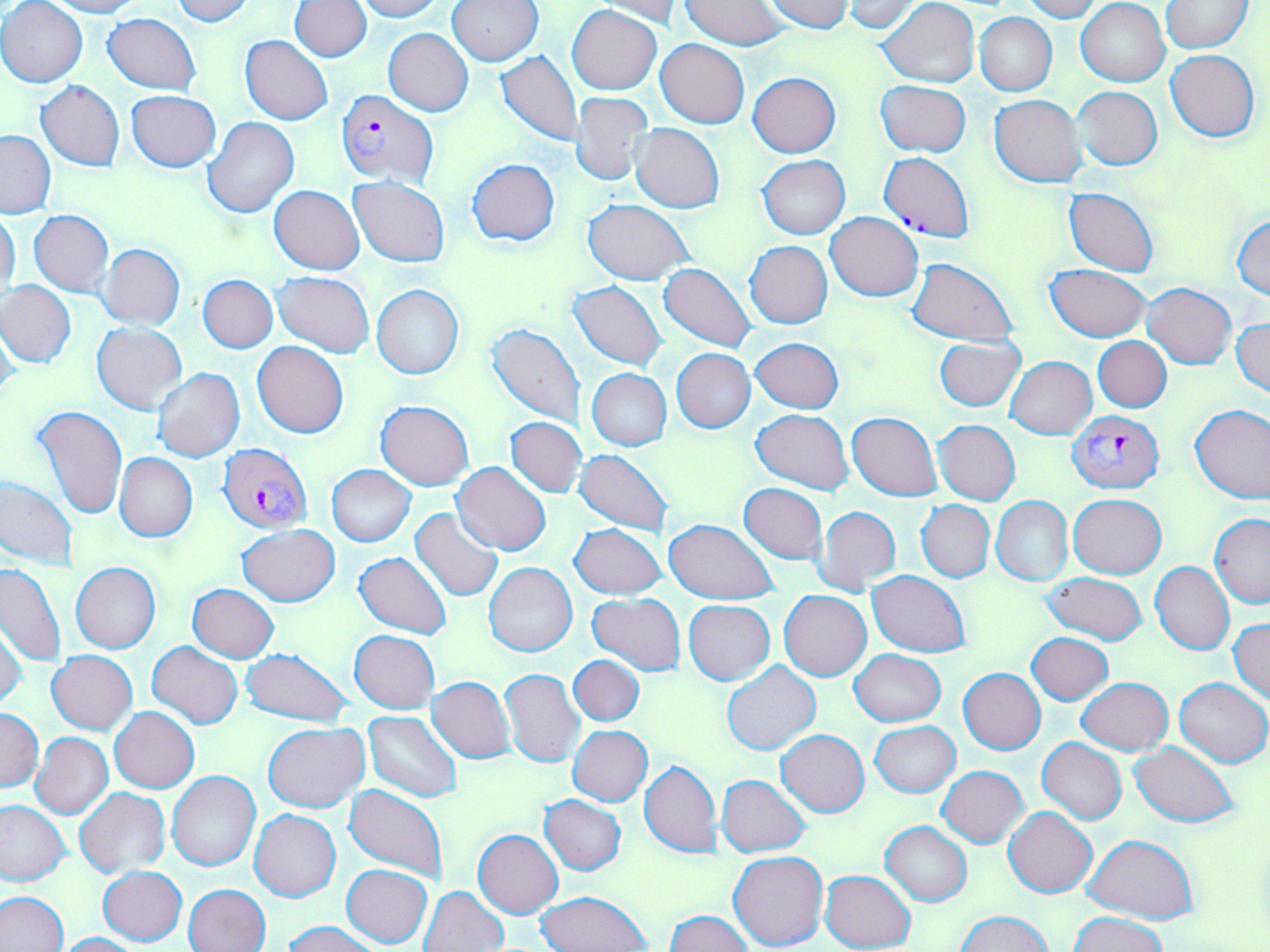 Approximate bounding boxes as [x1, y1, x2, y2] in pixels. Plasmodium falciparum-infected red blood cell locations: [336, 89, 438, 189], [1067, 413, 1164, 494], [225, 449, 319, 540]. Uninfected red blood cell locations: [40, 0, 143, 18], [170, 0, 252, 26], [356, 0, 444, 21], [448, 0, 543, 65], [763, 0, 856, 34], [1018, 0, 1101, 22], [1, 1, 88, 87], [290, 1, 371, 62], [583, 1, 684, 29], [846, 1, 925, 33], [1076, 1, 1170, 86], [1160, 1, 1252, 52], [680, 2, 790, 50], [878, 2, 980, 87], [567, 4, 661, 95], [103, 12, 202, 95], [974, 13, 1057, 96], [383, 28, 473, 116], [240, 35, 334, 125], [656, 39, 749, 128], [1166, 49, 1259, 141], [496, 50, 582, 146], [748, 73, 841, 157], [876, 80, 970, 156], [36, 81, 124, 171], [1072, 87, 1162, 169], [126, 90, 222, 171], [571, 92, 654, 185], [989, 95, 1087, 187], [203, 117, 298, 218], [632, 123, 723, 213], [1, 130, 55, 219], [879, 151, 974, 243], [758, 155, 850, 239], [467, 158, 560, 247], [348, 176, 449, 266], [269, 185, 364, 274], [1064, 188, 1159, 276], [582, 199, 693, 285], [1, 209, 20, 298], [28, 211, 114, 295], [825, 212, 923, 301], [1231, 214, 1270, 300], [745, 241, 833, 329], [98, 243, 185, 329], [907, 258, 1018, 344], [659, 263, 756, 351], [1046, 265, 1150, 341], [273, 271, 374, 356], [198, 274, 278, 352], [1, 279, 75, 368], [570, 281, 667, 369], [1141, 282, 1236, 368], [371, 284, 463, 379], [1233, 317, 1270, 397], [0, 318, 21, 409], [486, 322, 585, 427], [92, 323, 187, 414], [1092, 336, 1171, 412], [934, 337, 1026, 411], [751, 338, 843, 413], [252, 341, 349, 438], [671, 348, 755, 433], [1007, 356, 1096, 439], [152, 368, 245, 463], [587, 368, 672, 450], [375, 400, 474, 490], [1190, 403, 1270, 504], [33, 404, 127, 520], [751, 410, 854, 493], [848, 412, 942, 500], [506, 417, 586, 498], [933, 420, 1020, 505], [576, 448, 674, 536], [114, 453, 197, 541], [453, 462, 551, 557], [326, 465, 416, 546], [0, 477, 77, 568], [739, 483, 827, 563], [1068, 494, 1166, 578], [991, 496, 1073, 585], [917, 499, 995, 582], [814, 505, 901, 596], [410, 508, 503, 602], [1209, 515, 1270, 608], [664, 518, 778, 606], [569, 524, 669, 599], [238, 525, 339, 606], [353, 551, 453, 639], [70, 561, 161, 653], [1150, 561, 1234, 655], [484, 562, 577, 657], [0, 564, 65, 665], [867, 571, 970, 656], [1042, 572, 1146, 644], [189, 584, 279, 662], [779, 590, 872, 682], [589, 593, 685, 675], [683, 600, 775, 684], [1229, 618, 1270, 702], [0, 623, 28, 712], [349, 629, 440, 713], [1026, 632, 1113, 704], [148, 642, 242, 729], [241, 647, 352, 727], [849, 649, 945, 727], [46, 651, 137, 735], [862, 651, 950, 797], [568, 655, 644, 726], [722, 661, 819, 755], [499, 668, 585, 768], [958, 668, 1045, 754], [427, 677, 515, 764], [1077, 677, 1173, 755], [1175, 678, 1269, 767], [109, 707, 198, 793], [0, 709, 44, 791], [363, 711, 461, 802], [870, 721, 960, 796], [262, 722, 369, 812], [569, 724, 651, 806], [776, 730, 869, 817], [29, 732, 114, 819], [1037, 738, 1127, 824], [1130, 742, 1240, 827], [639, 760, 720, 858], [937, 766, 1027, 847], [167, 771, 261, 872], [717, 774, 810, 857], [343, 785, 450, 885], [75, 788, 170, 878], [539, 795, 627, 874], [0, 799, 71, 887], [1004, 806, 1097, 898], [250, 809, 341, 901], [880, 820, 971, 906], [473, 829, 562, 918], [1082, 834, 1197, 923], [729, 851, 829, 951], [342, 863, 432, 948], [97, 865, 187, 945], [820, 869, 915, 952], [183, 884, 271, 952], [420, 885, 508, 951], [1, 891, 68, 952], [537, 891, 651, 952], [664, 910, 751, 952], [954, 912, 1055, 952], [1068, 912, 1169, 952], [284, 920, 381, 952], [55, 933, 141, 952]. Slide-level diagnosis: Plasmodium falciparum. Image is 1270×952 pixels. May-Grünwald-Giemsa stain. Light microscopy. Thin blood film. Captured at 1000x magnification. One field of a larger specimen.